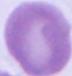

{
  "modality": "photomicrograph",
  "magnification": "1000x",
  "identification": "erythrocyte"
}